Locate every Plasmodium vivax-infected red blood cell.
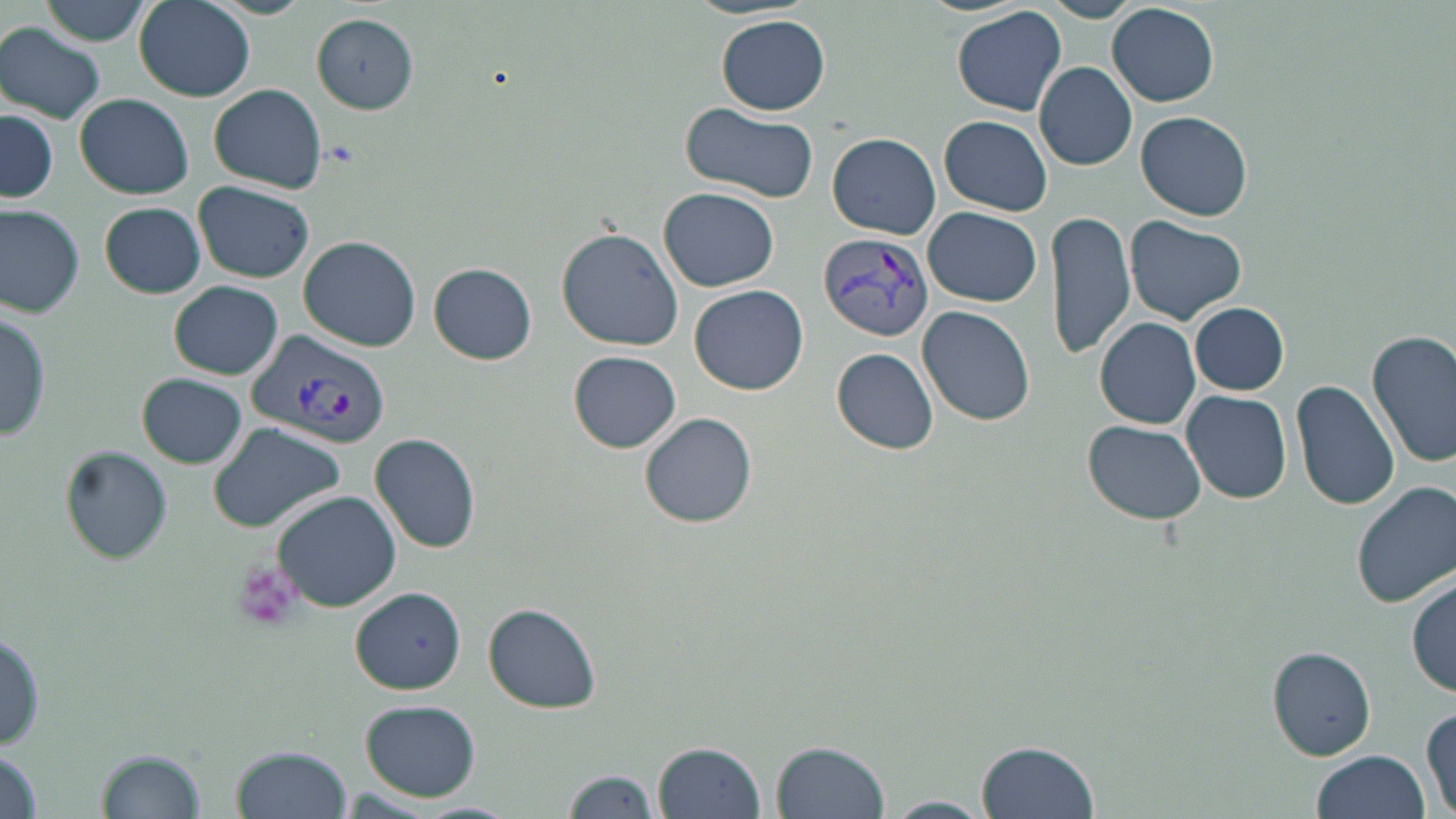
Approximate bounding boxes as (x1,y1)-(x2,y2) corner pairs in pixels.
Plasmodium vivax-infected red blood cells: (819,232)-(933,344), (248,330)-(391,451).

Uninfected red blood cell locations: (33,0)-(153,47), (1038,0)-(1147,22), (134,2)-(255,101), (1108,3)-(1220,107), (951,5)-(1066,116), (312,16)-(419,112), (716,16)-(831,115), (1,24)-(108,123), (1034,62)-(1136,171), (209,84)-(328,193), (75,92)-(194,198), (679,104)-(818,204), (1,108)-(57,204), (1137,110)-(1252,221), (938,114)-(1052,216), (827,132)-(941,239), (194,183)-(315,284), (660,187)-(779,290), (99,202)-(206,298), (923,205)-(1042,307), (0,206)-(84,316), (1048,207)-(1136,362), (1127,216)-(1247,324), (557,227)-(684,352), (299,238)-(420,351), (430,262)-(538,363), (170,280)-(282,379), (691,284)-(807,396), (1189,302)-(1289,395), (917,305)-(1037,427), (0,309)-(52,444), (1096,318)-(1201,429), (1368,331)-(1456,470), (830,347)-(940,455), (568,350)-(682,453), (138,373)-(245,467), (1291,379)-(1399,512), (1181,389)-(1294,503), (640,412)-(758,528), (1083,419)-(1207,524), (209,421)-(346,532), (371,434)-(479,552), (62,446)-(172,563), (1352,481)-(1456,609), (272,490)-(402,612), (1410,576)-(1455,699), (351,587)-(466,692), (484,604)-(601,712), (1,627)-(47,752), (1268,647)-(1376,759), (361,700)-(480,800), (1422,705)-(1456,816), (975,736)-(1099,816), (771,738)-(892,819), (653,739)-(768,819), (231,746)-(351,819), (98,747)-(204,819), (0,749)-(46,819), (1311,751)-(1430,819), (561,767)-(661,819), (882,795)-(996,818), (411,801)-(522,819). Platelet locations: (231,560)-(306,634). Slide-level diagnosis: Plasmodium vivax. Optical microscopy. Image is 1456×819 pixels. 1000x magnification. Thin blood film. May-Grünwald-Giemsa-stained preparation. Single field of view.